Assess this cell for malaria.
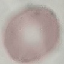

Uninfected.

Giemsa-stained preparation. Automatically extracted cell patch, resized to 64 × 64 pixels. Thin blood film. Acquired by smartphone through the microscope eyepiece.